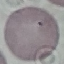

Summary:
  - Result: no malaria parasites detected
  - Preparation: thin blood smear
  - Capture: smartphone through the microscope eyepiece
  - Stain: Giemsa
  - Image type: automatically extracted cell patch, resized to 64 × 64 pixels